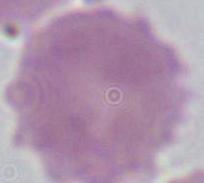
Captured at 1000x magnification. Micrograph. An erythrocyte is seen.